Classify this cell by malaria status.
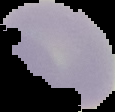
Uninfected.

Segmented cell region on a black background. From a thin blood film. Image is 115×112 pixels.